Report the malaria status.
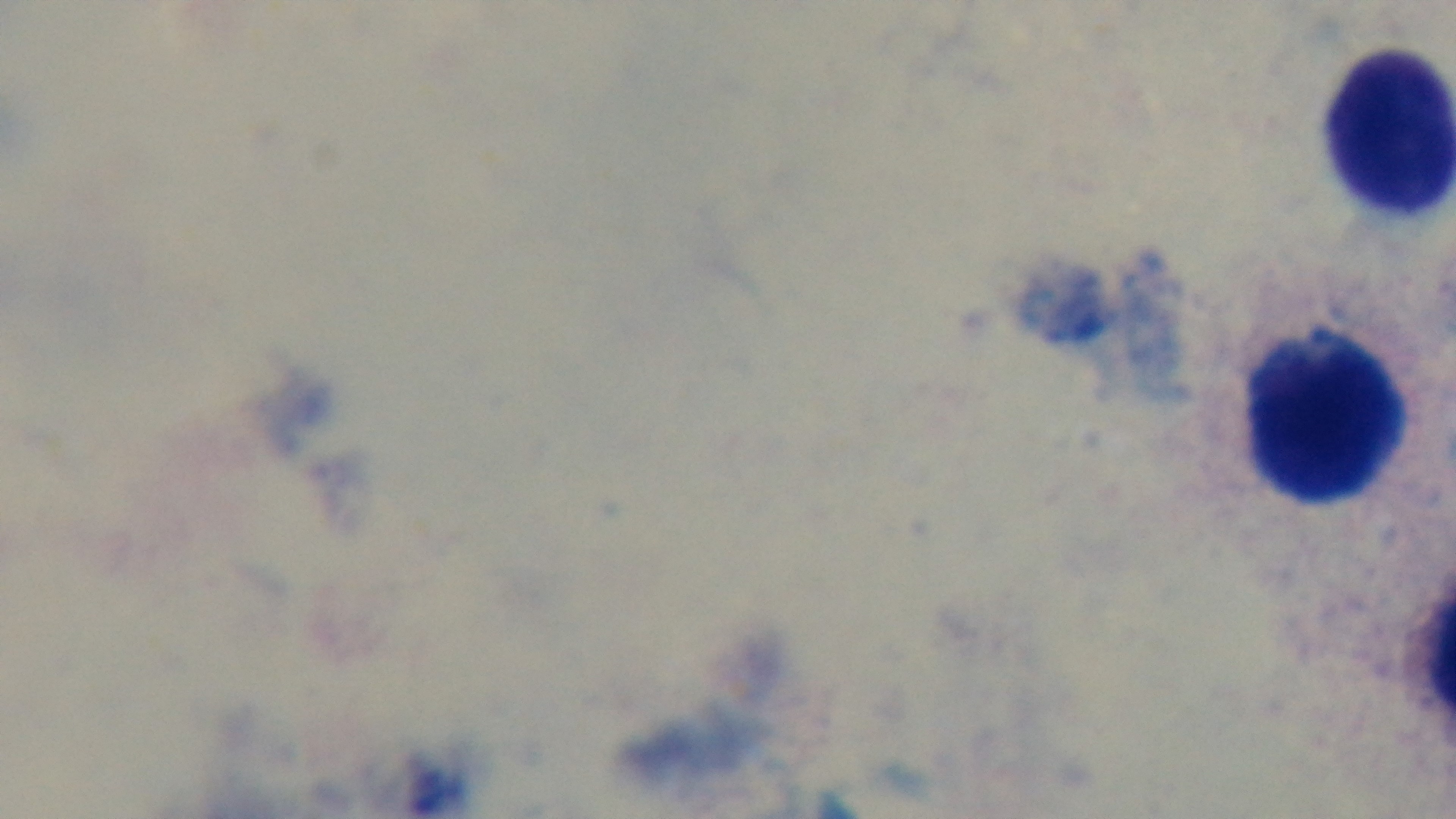

Uninfected.

Summary:
  - Objective: 100x oil immersion
  - Field of view: one from the slide
  - Modality: light microscopy
  - Preparation: thick
  - Stain: Giemsa
  - Capture: mounted 4K digital camera